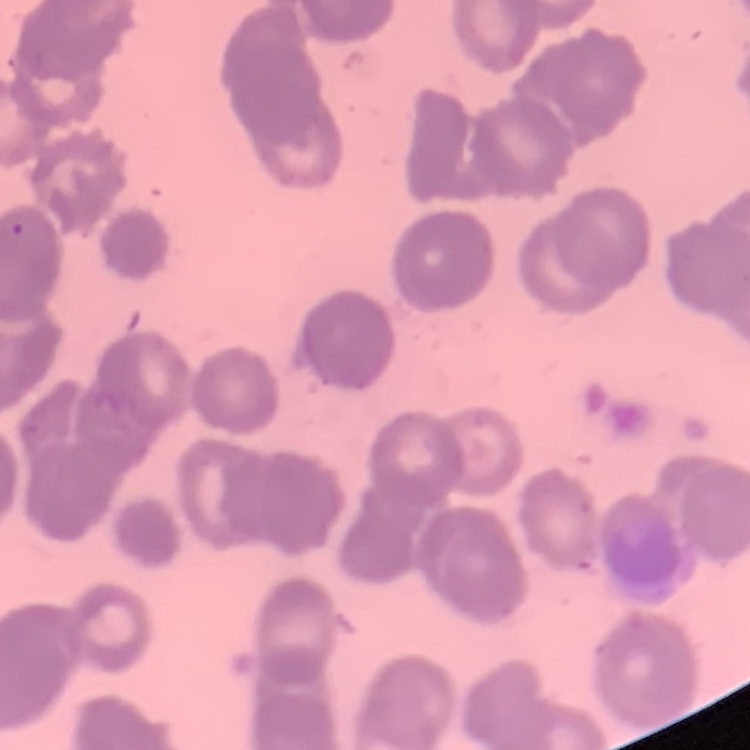
erythrocyte morphology = rouleaux formation
image type = one tile cut from a larger photomicrograph
preparation = thin blood film
stain = Field's or Giemsa